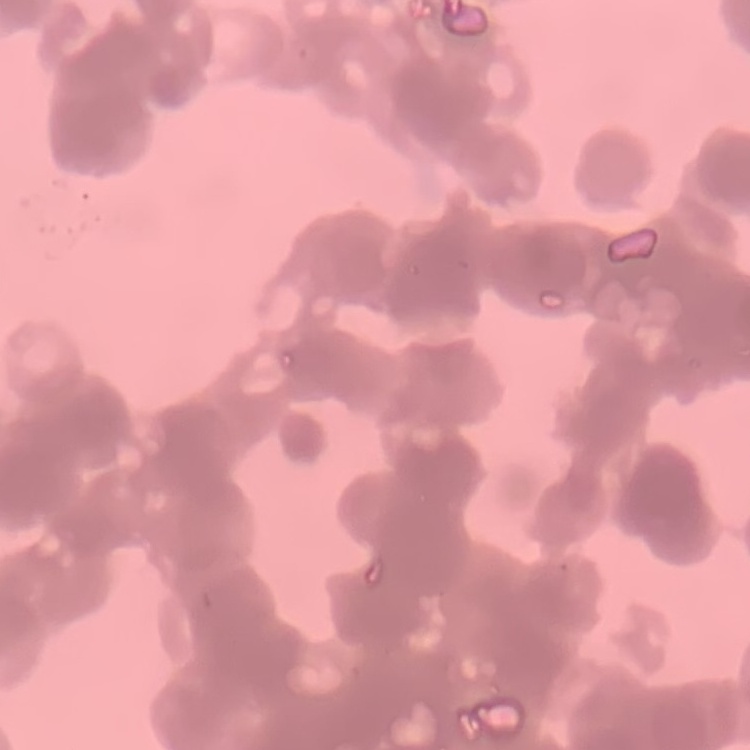
Summary:
  - Red blood cell morphology: rouleaux formation
  - Preparation: thin blood film
  - Image type: square crop of a larger photomicrograph
  - Stain: Field's or Giemsa